Evaluate for Plasmodium parasites.
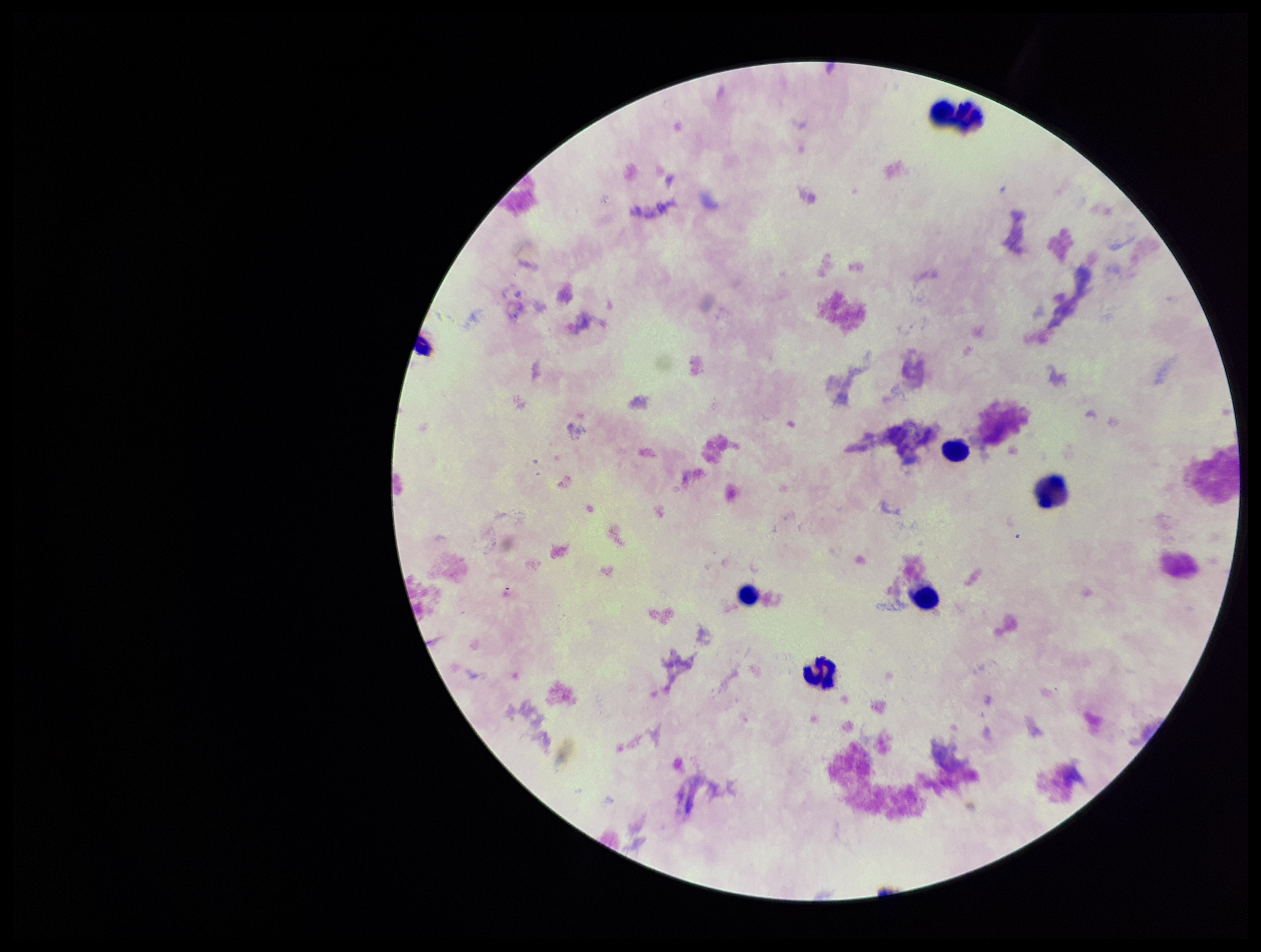

None identified.

Summary:
  - Preparation: thick blood smear
  - Patient malaria status: negative
  - Field of view: one from this slide
  - Leukocyte count: 7
  - Parasite count: 0
  - Stain: Giemsa
  - Capture: smartphone photograph through the microscope eyepiece
  - Image size: 1261×952 pixels